Classify this cell by malaria status.
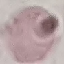

Uninfected.

Summary:
  - Capture: smartphone through the microscope eyepiece
  - Preparation: thin smear
  - Image type: cell patch, automatically extracted from a larger field of view and resized to 64 × 64 pixels
  - Stain: Giemsa